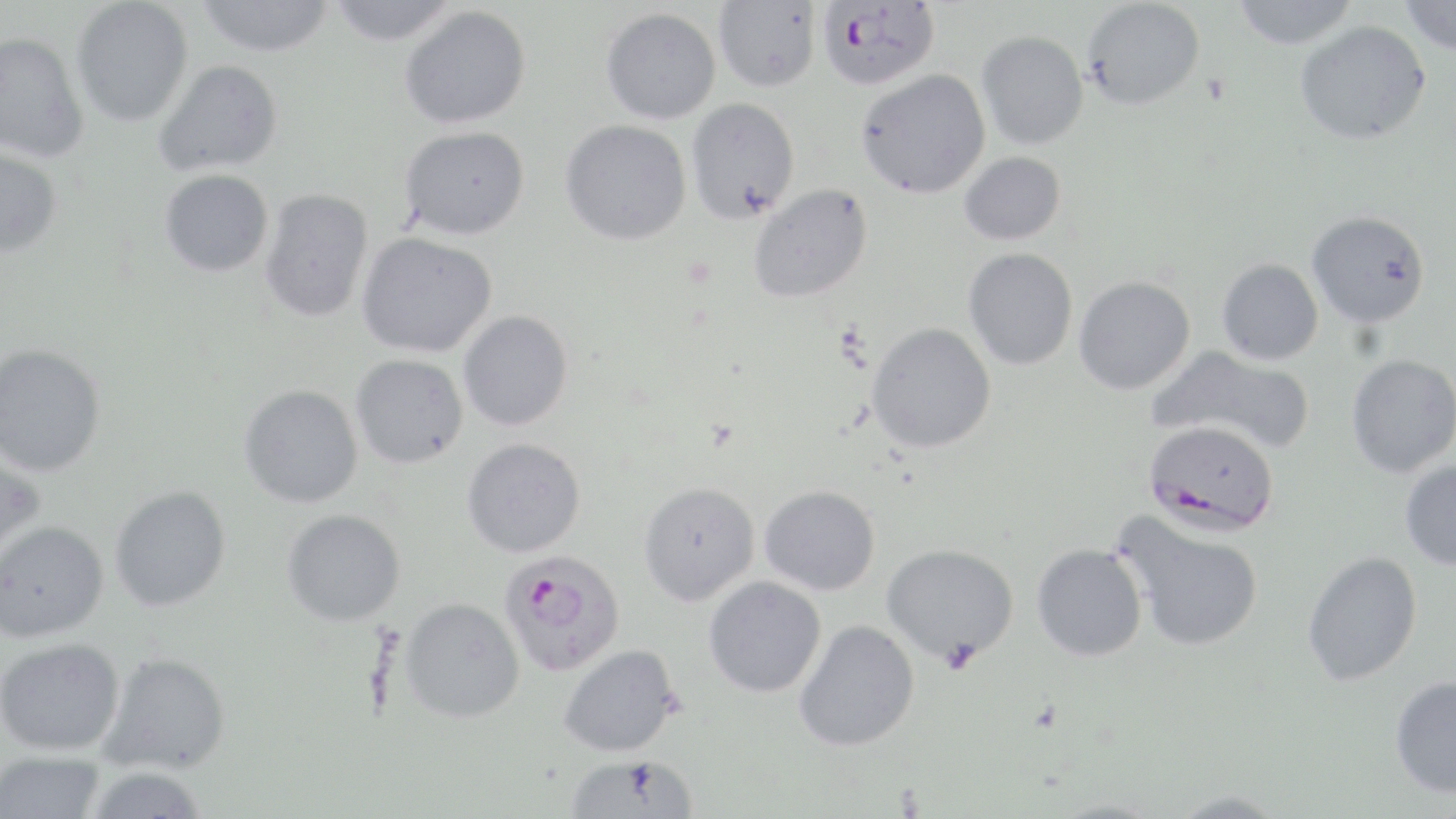
Approximate bounding boxes as named x1/y1/x2/y2 corners in pixels. Plasmodium falciparum-infected red blood cell locations: (x1=816, y1=1, x2=940, y2=90), (x1=1143, y1=419, x2=1280, y2=537), (x1=499, y1=549, x2=626, y2=676). Uninfected red blood cell locations: (x1=195, y1=0, x2=335, y2=57), (x1=1080, y1=0, x2=1205, y2=110), (x1=1230, y1=0, x2=1360, y2=48), (x1=1398, y1=0, x2=1456, y2=56), (x1=71, y1=1, x2=194, y2=127), (x1=326, y1=1, x2=461, y2=46), (x1=713, y1=1, x2=821, y2=92), (x1=399, y1=5, x2=531, y2=129), (x1=600, y1=7, x2=721, y2=124), (x1=1295, y1=20, x2=1431, y2=145), (x1=976, y1=30, x2=1089, y2=151), (x1=0, y1=31, x2=89, y2=163), (x1=154, y1=59, x2=283, y2=176), (x1=855, y1=70, x2=991, y2=198), (x1=686, y1=98, x2=800, y2=224), (x1=560, y1=119, x2=692, y2=245), (x1=400, y1=126, x2=530, y2=240), (x1=0, y1=145, x2=63, y2=257), (x1=959, y1=152, x2=1066, y2=246), (x1=159, y1=169, x2=274, y2=277), (x1=748, y1=184, x2=872, y2=304), (x1=259, y1=189, x2=375, y2=323), (x1=1306, y1=210, x2=1430, y2=328), (x1=357, y1=233, x2=497, y2=358), (x1=963, y1=248, x2=1078, y2=371), (x1=1217, y1=259, x2=1324, y2=365), (x1=1074, y1=276, x2=1195, y2=395), (x1=458, y1=311, x2=573, y2=431), (x1=866, y1=322, x2=997, y2=453), (x1=0, y1=343, x2=107, y2=477), (x1=1148, y1=345, x2=1316, y2=454), (x1=350, y1=354, x2=468, y2=468), (x1=1346, y1=354, x2=1456, y2=478), (x1=239, y1=384, x2=363, y2=508), (x1=462, y1=437, x2=586, y2=557), (x1=0, y1=452, x2=46, y2=567), (x1=1400, y1=460, x2=1456, y2=570), (x1=638, y1=481, x2=760, y2=606), (x1=759, y1=484, x2=880, y2=595), (x1=109, y1=485, x2=231, y2=612), (x1=282, y1=508, x2=406, y2=626), (x1=1113, y1=512, x2=1266, y2=653), (x1=0, y1=520, x2=109, y2=643), (x1=881, y1=543, x2=1019, y2=665), (x1=1032, y1=543, x2=1148, y2=661), (x1=1302, y1=550, x2=1423, y2=686), (x1=703, y1=576, x2=826, y2=698), (x1=400, y1=597, x2=526, y2=723), (x1=793, y1=620, x2=920, y2=752), (x1=0, y1=637, x2=125, y2=756), (x1=558, y1=644, x2=680, y2=756), (x1=101, y1=651, x2=232, y2=774), (x1=1389, y1=675, x2=1456, y2=798), (x1=0, y1=752, x2=106, y2=818), (x1=565, y1=753, x2=700, y2=817), (x1=83, y1=766, x2=210, y2=819), (x1=1166, y1=790, x2=1290, y2=818). Slide-level diagnosis: Plasmodium falciparum. Captured at 1000x magnification. Thin blood smear. Optical microscopy. Image is 1456×819 pixels. May-Grünwald-Giemsa-stained preparation. Single field of view.